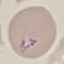 Malaria status: parasitized. Automatically extracted cell patch, resized to 64 × 64 pixels. Giemsa-stained preparation. Thin blood smear. Photographed with a smartphone camera at the microscope eyepiece.